Name the parasite shown.
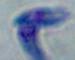

This is Toxoplasma gondii.

Summary:
  - Magnification: 1000x
  - Modality: photomicrograph